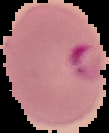

Malaria status: parasitized. Image is 109×133 pixels. From a thin blood film. The area outside the segmented cell region is set to black.